Name the cell type shown.
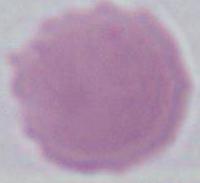

An erythrocyte.

magnification = 1000x
modality = micrograph